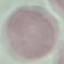

Malaria status: uninfected. Giemsa-stained preparation. Acquired by smartphone through the microscope eyepiece. Thin smear of blood. Automatically extracted cell patch, resized to 64 × 64 pixels.